Locate every uninfected red blood cell.
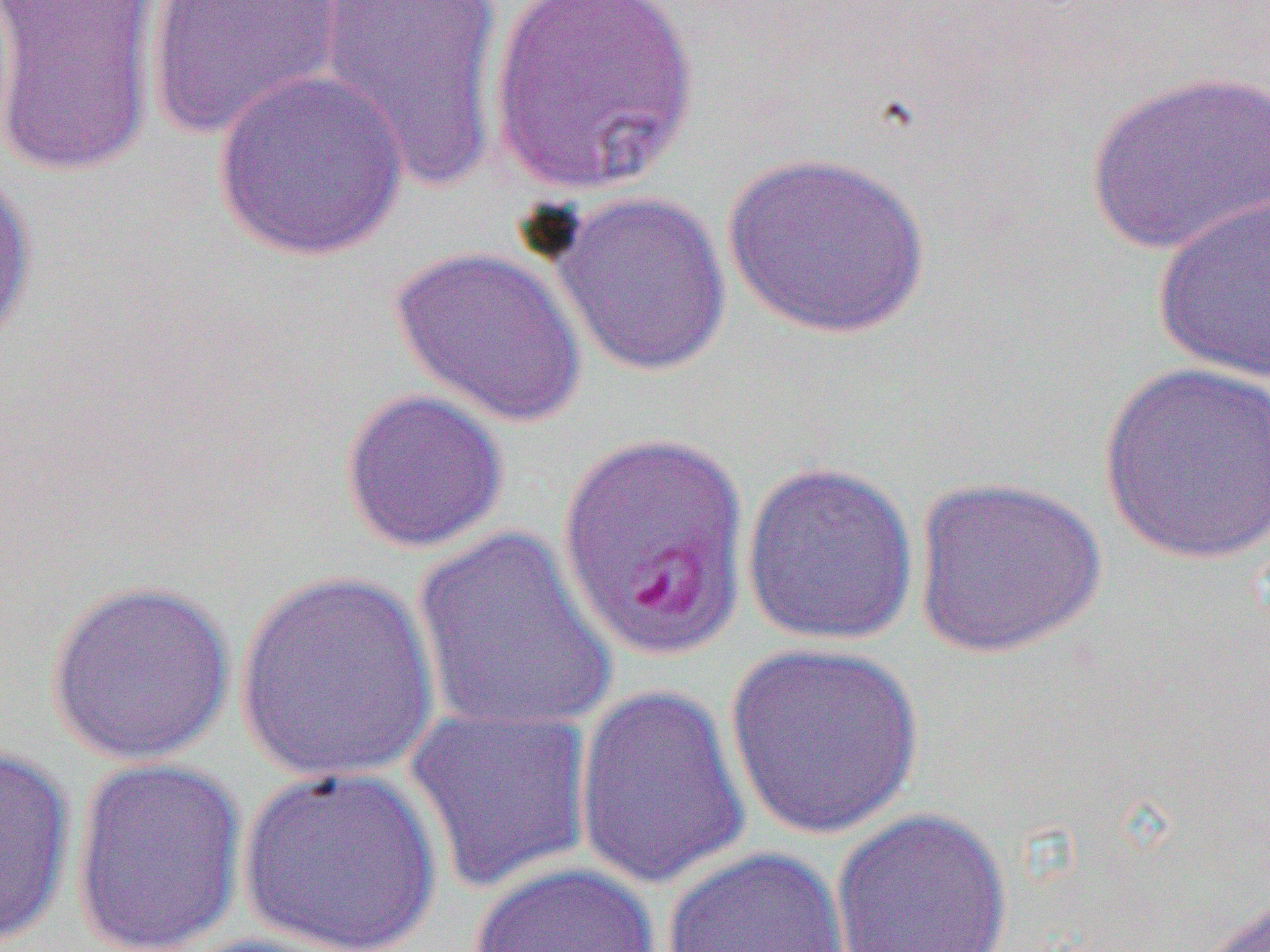
Approximate bounding boxes as [x1, y1, x2, y2] in pixels.
Uninfected red blood cells: [144, 0, 345, 142], [312, 0, 509, 191], [489, 0, 699, 195], [0, 2, 161, 179], [211, 68, 409, 261], [1085, 69, 1270, 259], [722, 151, 934, 340], [0, 167, 38, 353], [549, 190, 732, 378], [1151, 195, 1270, 384], [389, 245, 588, 429], [1098, 361, 1270, 565], [339, 388, 510, 554], [740, 460, 919, 647], [910, 475, 1107, 658], [412, 527, 620, 735], [234, 569, 442, 786], [45, 579, 237, 766], [724, 641, 925, 840], [572, 684, 752, 892], [404, 705, 595, 896], [0, 744, 76, 949], [69, 756, 249, 952], [237, 765, 443, 952], [830, 807, 1013, 952], [661, 846, 851, 952], [467, 861, 661, 952], [1194, 893, 1270, 952], [171, 932, 360, 952].

Summary:
  - Slide-level diagnosis: Plasmodium falciparum
  - Modality: optical microscopy
  - Field of view: one of a larger specimen
  - Magnification: 1000x
  - Preparation: thin blood smear
  - Image size: 1270×952 pixels